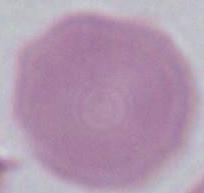
An erythrocyte is shown. 1000x magnification. Photomicrograph.